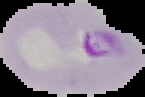
Summary:
  - Malaria status: parasitized
  - Image type: segmented cell region with the area outside set to black
  - Preparation: thin blood film
  - Image size: 145×97 pixels